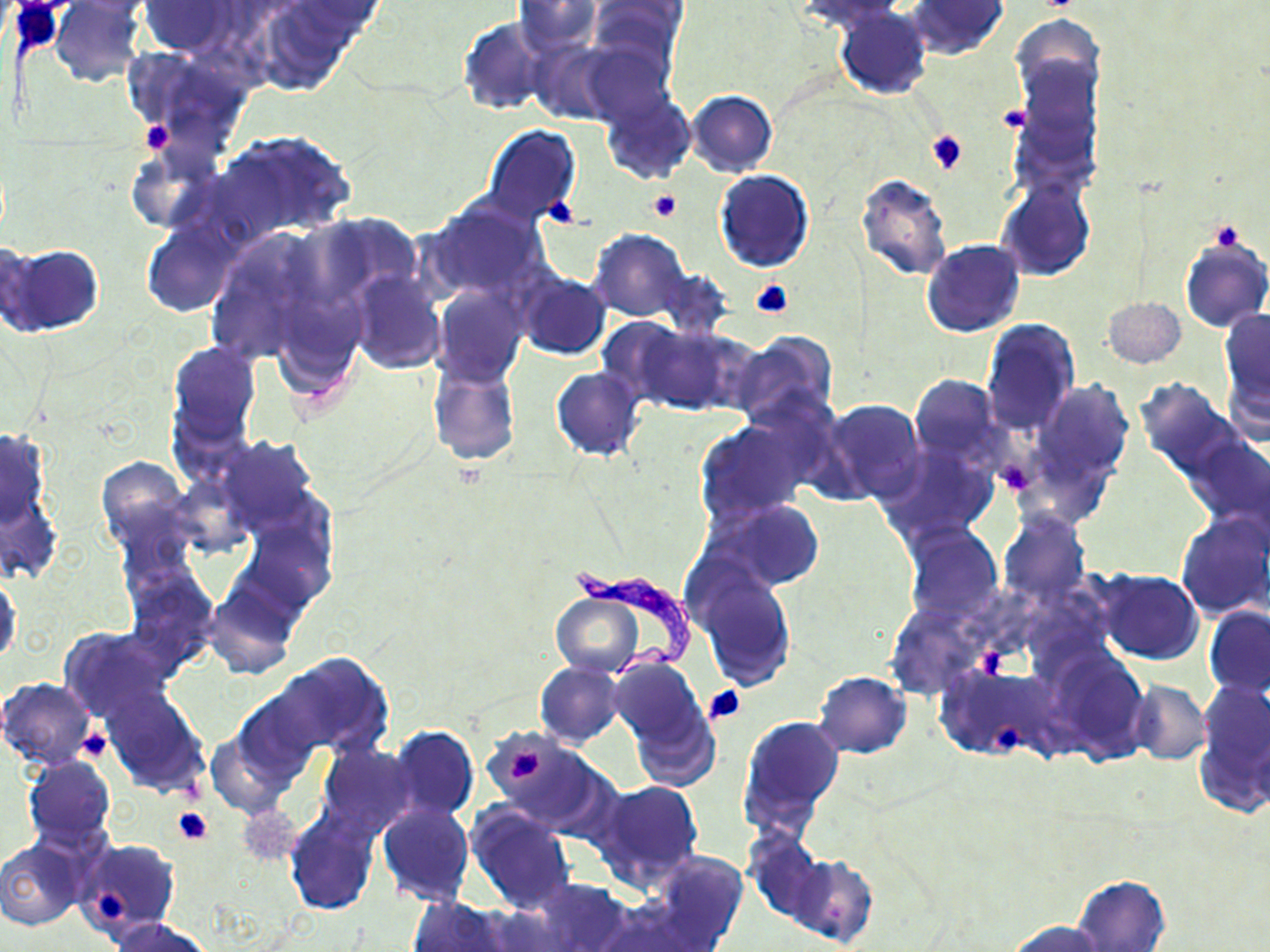 Approximate bounding boxes as (x1,y1)-(x2,y2) corner pairs in pixels. Trypanosoma brucei locations: (573,562)-(699,675). Platelet locations: (997,104)-(1031,133), (139,121)-(172,154), (927,130)-(969,174), (648,188)-(682,223), (543,196)-(580,227), (1209,221)-(1245,251), (750,280)-(794,318), (993,452)-(1039,497), (976,643)-(1008,681), (703,685)-(745,725), (994,721)-(1025,753), (75,729)-(111,762), (508,747)-(550,780), (173,807)-(214,846), (95,887)-(130,921). Uninfected red blood cell locations: (50,0)-(147,87), (59,0)-(155,20), (514,0)-(601,55), (588,0)-(684,68), (909,0)-(1008,58), (797,1)-(907,30), (139,2)-(237,57), (248,6)-(357,96), (835,6)-(932,99), (1011,13)-(1104,109), (458,17)-(551,116), (526,38)-(618,124), (579,39)-(676,126), (122,45)-(257,152), (1012,54)-(1102,185), (599,90)-(694,186), (687,90)-(778,176), (484,125)-(581,226), (214,130)-(355,244), (124,142)-(223,234), (714,169)-(814,272), (855,173)-(953,280), (998,178)-(1094,280), (425,198)-(552,304), (141,223)-(238,318), (200,228)-(331,367), (591,230)-(690,321), (1179,235)-(1270,333), (0,239)-(41,334), (922,239)-(1025,338), (2,244)-(105,335), (656,268)-(734,338), (349,271)-(446,374), (516,273)-(612,360), (433,286)-(527,386), (1102,296)-(1186,369), (1219,309)-(1270,406), (595,315)-(701,407), (981,318)-(1079,435), (630,322)-(750,415), (730,332)-(839,430), (167,341)-(260,448), (427,361)-(519,467), (1223,365)-(1270,448), (551,367)-(646,461), (909,374)-(1002,464), (1134,378)-(1242,481), (1037,380)-(1133,479), (820,398)-(926,504), (694,419)-(812,526), (0,429)-(50,528), (1183,434)-(1270,531), (218,435)-(318,529), (878,446)-(996,544), (95,456)-(191,555), (711,500)-(823,591), (998,510)-(1090,607), (1176,511)-(1270,620), (246,512)-(336,611), (904,523)-(1001,627), (124,565)-(217,670), (692,565)-(798,688), (1096,570)-(1203,663), (0,575)-(21,664), (205,583)-(297,682), (553,591)-(643,678), (1204,606)-(1270,697), (60,627)-(176,724), (1048,646)-(1144,761), (267,653)-(390,757), (607,654)-(707,751), (535,661)-(625,747), (937,663)-(1049,760), (815,670)-(910,757), (0,677)-(98,769), (1195,677)-(1270,815), (1128,680)-(1212,764), (104,691)-(208,794), (231,691)-(320,785), (628,698)-(718,791), (737,713)-(845,840), (389,725)-(478,822), (486,730)-(610,833), (206,732)-(293,818), (317,745)-(416,838), (22,755)-(116,854), (590,779)-(704,889), (377,803)-(475,905), (466,803)-(574,913), (236,806)-(302,867), (285,810)-(379,915), (743,833)-(827,925), (70,839)-(179,940), (0,840)-(85,929), (652,851)-(746,947), (789,856)-(877,948), (1072,875)-(1170,952), (530,878)-(634,952), (408,896)-(512,952), (109,917)-(212,952), (1006,919)-(1111,952). Slide-level diagnosis: Trypanosoma brucei. Image is 1270×952 pixels. May-Grünwald-Giemsa stain. Thin blood film. Single field of view. 1000x magnification. Light microscopy.